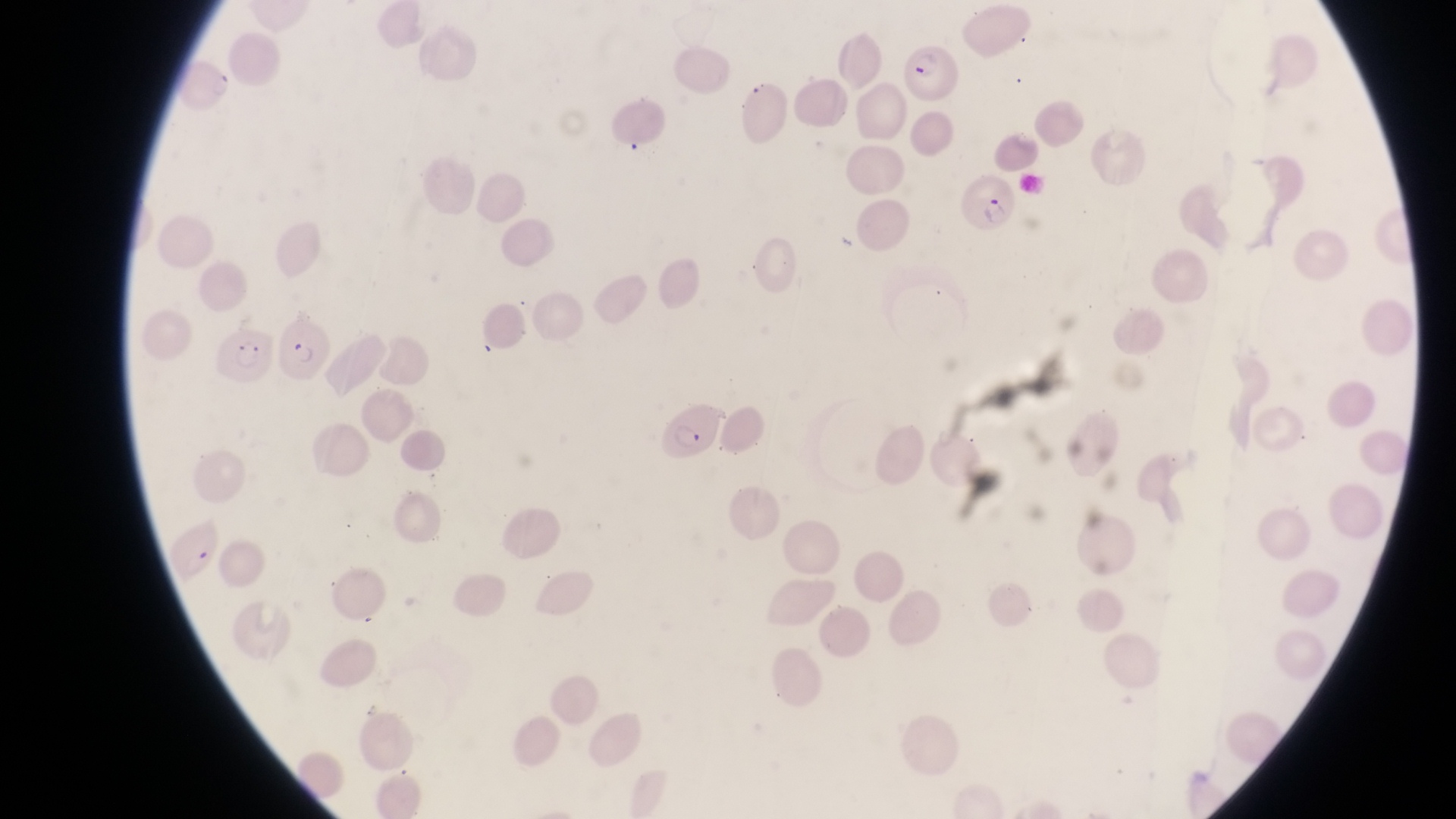
Approximate bounding boxes as {left, top, right, bottom} in pixels. Parasitised red blood cell locations: {904, 37, 963, 103}, {959, 171, 1023, 235}, {275, 317, 331, 386}, {215, 325, 273, 385}, {660, 397, 721, 463}, {164, 522, 224, 582}. Captured by a smartphone held over the eyepiece of an Olympus CX-23 microscope. Thin blood film. Image is 1456×819 pixels. Single field of view. Sample from Uganda. At a magnification of 1000x.